Identify the blood parasite species.
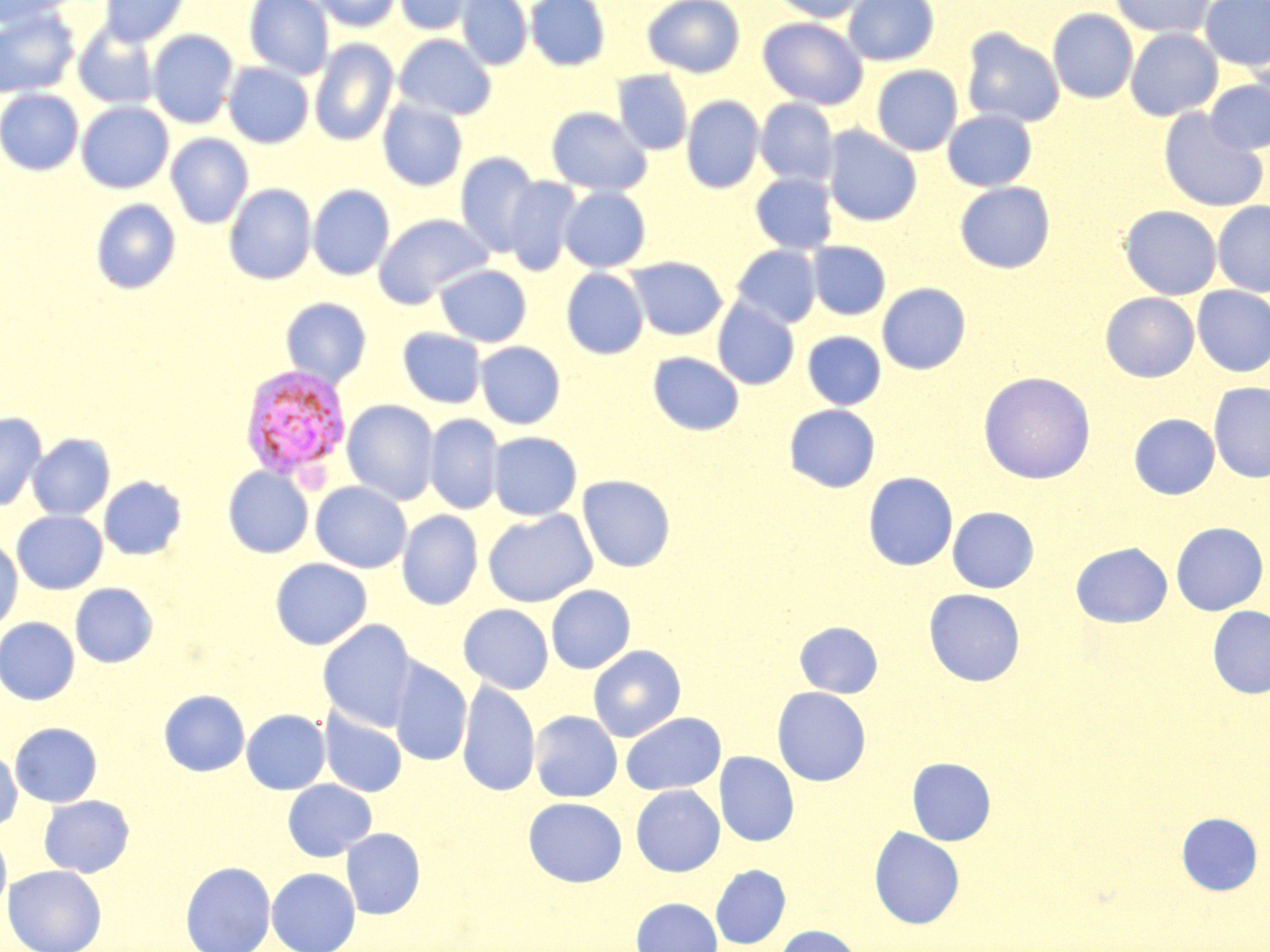

Plasmodium vivax.

Approximate bounding boxes as [x1, y1, x2, y2] in pixels. Plasmodium vivax-infected red blood cell locations: [239, 363, 351, 484]. Uninfected red blood cell locations: [0, 0, 77, 26], [98, 0, 190, 47], [244, 0, 333, 80], [311, 0, 402, 32], [394, 0, 479, 35], [456, 0, 532, 70], [525, 0, 610, 71], [643, 0, 745, 78], [767, 0, 871, 23], [843, 0, 939, 66], [1109, 0, 1214, 38], [1200, 0, 1270, 71], [0, 7, 80, 98], [1047, 8, 1138, 104], [758, 16, 868, 110], [73, 25, 160, 110], [961, 27, 1065, 128], [1125, 28, 1223, 121], [147, 29, 238, 129], [393, 34, 497, 120], [309, 39, 398, 146], [223, 62, 314, 148], [871, 65, 963, 156], [613, 70, 693, 155], [1205, 77, 1270, 155], [0, 89, 84, 175], [682, 95, 764, 193], [756, 98, 839, 187], [377, 99, 467, 191], [76, 101, 173, 193], [546, 107, 652, 196], [1157, 108, 1268, 211], [942, 109, 1037, 191], [823, 125, 922, 226], [165, 133, 254, 229], [456, 152, 542, 257], [750, 173, 838, 254], [503, 176, 582, 276], [955, 182, 1055, 273], [224, 183, 316, 285], [308, 184, 394, 280], [560, 186, 651, 272], [90, 199, 181, 294], [1213, 201, 1270, 296], [1119, 205, 1221, 299], [373, 213, 493, 307], [807, 241, 891, 320], [730, 245, 821, 329], [625, 256, 727, 340], [435, 264, 531, 347], [561, 268, 649, 359], [877, 283, 971, 374], [1192, 286, 1270, 377], [1100, 292, 1199, 382], [280, 297, 372, 387], [712, 299, 799, 390], [398, 328, 486, 408], [802, 331, 886, 409], [475, 341, 565, 429], [648, 352, 744, 435], [977, 371, 1096, 484], [1208, 382, 1270, 482], [342, 399, 439, 505], [783, 404, 880, 493], [0, 411, 47, 512], [1129, 413, 1220, 499], [424, 414, 503, 515], [488, 431, 582, 520], [27, 433, 115, 520], [223, 467, 313, 558], [863, 472, 958, 571], [577, 474, 676, 572], [99, 476, 187, 560], [310, 481, 412, 573], [940, 506, 1035, 681], [947, 506, 1039, 593], [483, 509, 597, 607], [11, 510, 107, 595], [397, 510, 483, 610], [1170, 522, 1268, 615], [0, 538, 23, 634], [1070, 542, 1172, 628], [270, 557, 372, 650], [70, 583, 158, 667], [546, 585, 636, 674], [923, 588, 1025, 686], [458, 604, 554, 693], [1207, 605, 1270, 698], [0, 617, 80, 705], [317, 619, 419, 731], [793, 621, 884, 698], [588, 644, 687, 742], [388, 659, 472, 767], [457, 680, 540, 797], [772, 687, 871, 786], [158, 690, 250, 777], [319, 707, 407, 797], [242, 709, 330, 794], [530, 710, 622, 802], [620, 712, 726, 795], [10, 722, 102, 807], [0, 748, 22, 833], [715, 752, 799, 846], [907, 757, 996, 846], [282, 779, 377, 862], [630, 785, 725, 876], [39, 795, 135, 878], [523, 797, 628, 887], [1176, 812, 1263, 896], [868, 826, 965, 929], [341, 828, 425, 919], [0, 829, 12, 917], [180, 861, 275, 952], [710, 864, 791, 949], [3, 865, 106, 952], [267, 867, 360, 952], [631, 898, 722, 952], [774, 925, 863, 952]. May-Grünwald-Giemsa-stained preparation. Single field of view. Captured at 1000x magnification. Image is 1270×952 pixels. Optical microscopy. Thin blood film.